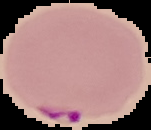
preparation: thin blood smear
image_type: cell region segmented out of the field of view; surrounding area masked to black
result: Plasmodium parasites identified
image_size: 151×130 pixels